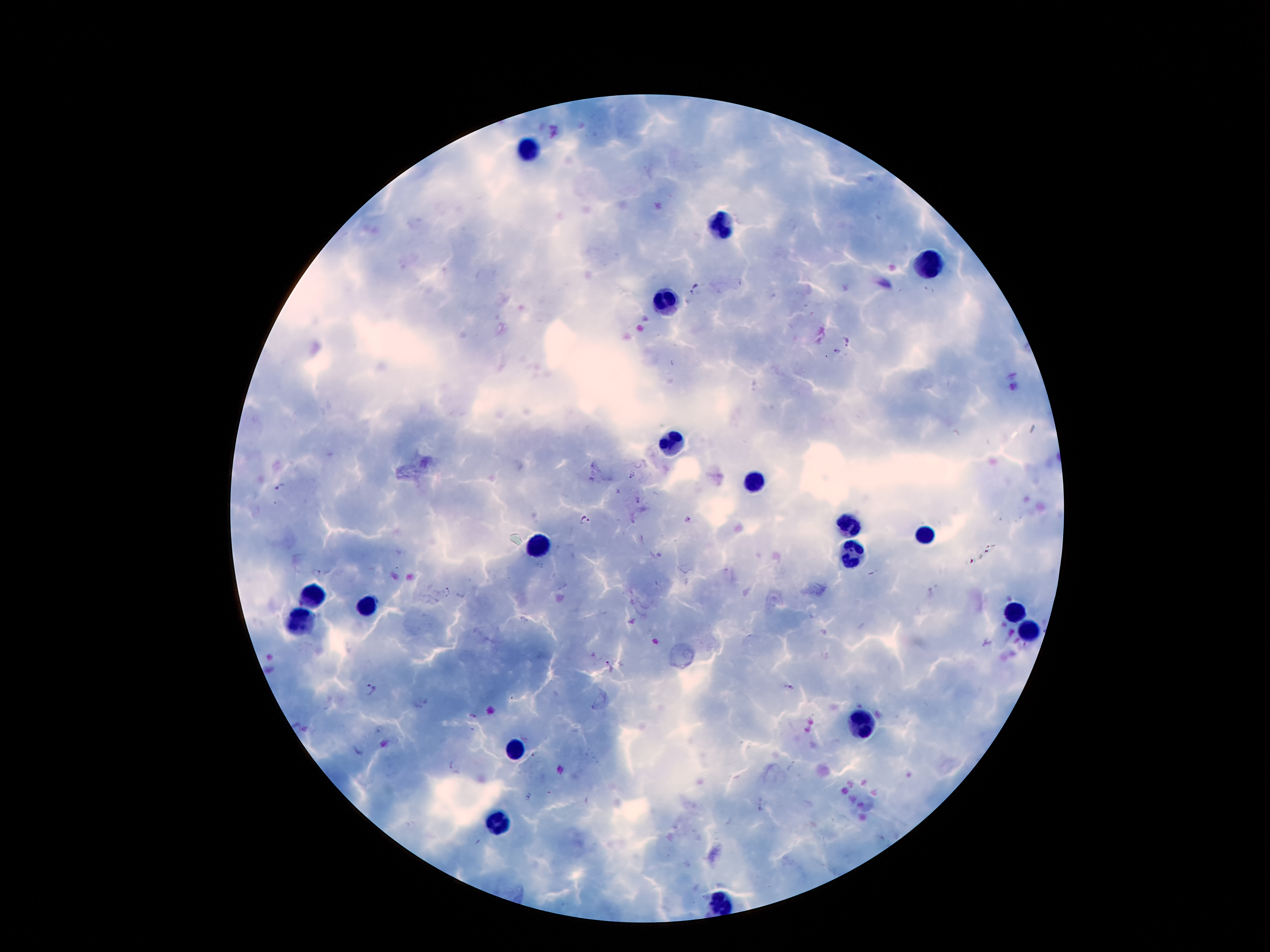 Approximate centers as {x, y} in pixels. Plasmodium parasite locations: {695, 289}, {847, 343}, {837, 353}, {632, 475}, {280, 487}, {585, 520}, {689, 520}, {660, 554}, {317, 574}, {448, 591}, {607, 667}, {788, 687}, {372, 689}, {533, 755}, {530, 797}. Leukocyte locations: {529, 153}, {722, 220}, {930, 264}, {663, 304}, {676, 445}, {755, 481}, {848, 527}, {927, 533}, {539, 546}, {852, 552}, {310, 598}, {369, 602}, {1014, 611}, {300, 621}, {1026, 632}, {865, 722}, {516, 749}, {499, 821}, {722, 903}. Patient malaria status: positive for Plasmodium falciparum. Giemsa-stained preparation. Image is 1270×952 pixels. 100x magnification. Thick peripheral-blood smear. Smartphone photograph taken through the microscope eyepiece. Single field of view.